Identify the parasite.
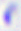

Toxoplasma gondii.

Summary:
  - Magnification: 400x
  - Modality: micrograph